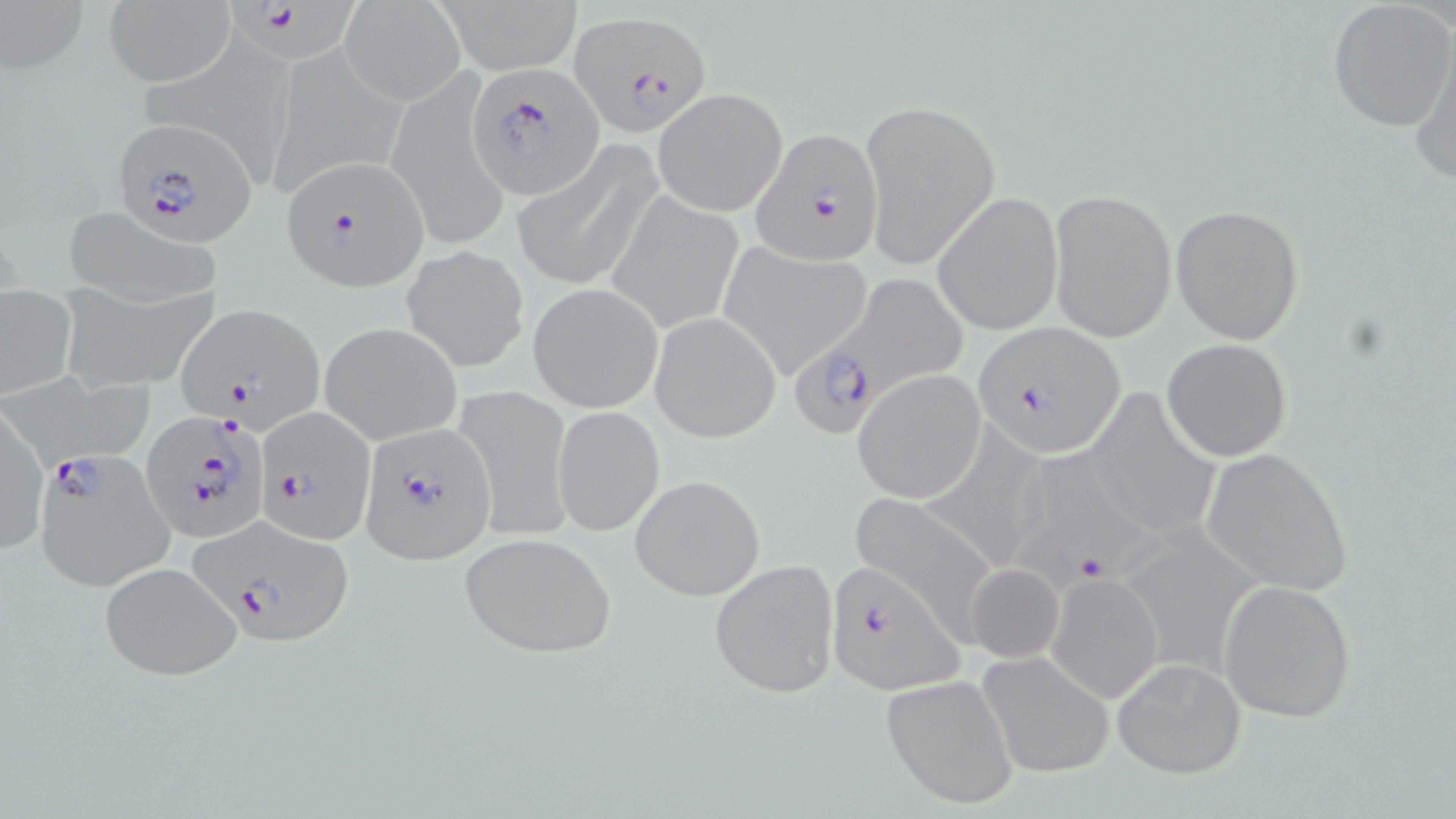

Summary:
  - Coordinate format: approximate bounding boxes as (x1, y1, x2, y2) in pixels
  - Plasmodium falciparum-infected red blood cell locations: (220, 0, 371, 72), (571, 9, 714, 138), (467, 62, 602, 199), (107, 119, 260, 243), (751, 128, 883, 266), (282, 156, 430, 291), (792, 269, 968, 437), (173, 302, 325, 430), (971, 323, 1126, 457), (254, 401, 373, 544), (143, 410, 269, 541), (361, 422, 497, 564), (34, 450, 177, 593), (1011, 457, 1166, 594), (192, 515, 355, 646), (823, 562, 963, 694)
  - Uninfected red blood cell locations: (0, 0, 91, 80), (432, 0, 582, 73), (1327, 1, 1456, 134), (103, 3, 234, 86), (340, 3, 463, 104), (137, 31, 302, 186), (1410, 39, 1456, 191), (273, 40, 406, 197), (397, 71, 509, 245), (651, 87, 788, 217), (859, 98, 1000, 271), (514, 142, 662, 292), (1048, 188, 1177, 343), (608, 190, 745, 334), (933, 191, 1064, 336), (58, 204, 226, 308), (1171, 204, 1304, 343), (718, 241, 875, 377), (401, 243, 528, 370), (527, 282, 664, 413), (59, 283, 220, 395), (0, 284, 77, 399), (650, 311, 780, 443), (319, 321, 462, 446), (1161, 338, 1293, 461), (852, 368, 986, 504), (15, 369, 155, 466), (453, 383, 575, 543), (1085, 394, 1219, 544), (0, 405, 48, 554), (552, 405, 664, 535), (928, 424, 1052, 570), (1198, 447, 1355, 595), (629, 473, 766, 602), (847, 493, 999, 631), (1120, 525, 1260, 674), (459, 530, 618, 660), (709, 558, 841, 701), (98, 561, 245, 680), (964, 563, 1065, 663), (1046, 571, 1163, 703), (1218, 579, 1358, 723), (976, 651, 1114, 779), (1113, 657, 1248, 779), (881, 672, 1020, 811)
  - Slide-level diagnosis: Plasmodium falciparum
  - Image size: 1456×819 pixels
  - Preparation: thin blood film
  - Magnification: 1000x
  - Modality: light microscopy
  - Field of view: single
  - Stain: May-Grünwald-Giemsa